Locate every blood parasite and identify its species.
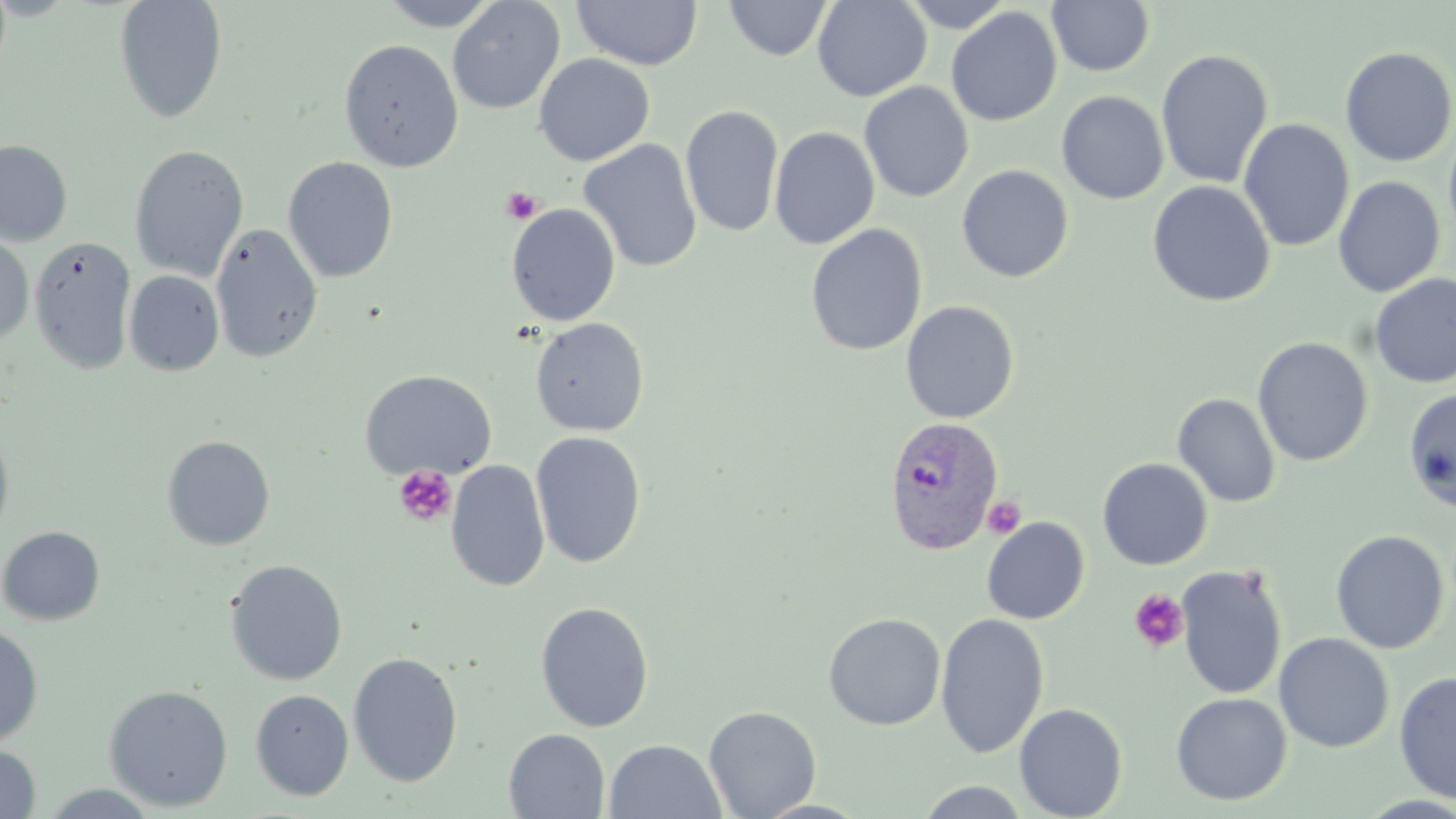
Approximate bounding boxes as (x1, y1, x2, y2) in pixels.
Plasmodium vivax-infected red blood cells: (883, 416, 1004, 554).
No Plasmodium falciparum, Plasmodium ovale, Plasmodium malariae, Babesia divergens, or Trypanosoma brucei observed.

Summary:
  - Platelet locations: (501, 186, 543, 225), (393, 465, 457, 527), (981, 495, 1026, 539), (1129, 589, 1189, 653)
  - Uninfected red blood cell locations: (379, 0, 500, 30), (447, 0, 565, 115), (724, 0, 833, 61), (812, 0, 932, 102), (899, 0, 1014, 33), (1047, 0, 1155, 77), (113, 1, 228, 123), (572, 1, 702, 70), (945, 6, 1063, 128), (338, 39, 464, 171), (1339, 45, 1456, 167), (1156, 48, 1273, 189), (533, 54, 655, 166), (858, 82, 974, 202), (1057, 91, 1169, 204), (680, 104, 784, 238), (1238, 119, 1354, 252), (1443, 120, 1456, 245), (769, 126, 880, 250), (0, 139, 73, 246), (578, 139, 703, 273), (129, 144, 249, 282), (283, 157, 399, 283), (956, 164, 1074, 283), (1333, 176, 1445, 298), (1148, 180, 1275, 307), (506, 204, 621, 326), (211, 223, 323, 364), (805, 224, 928, 356), (0, 231, 35, 345), (30, 235, 136, 374), (124, 270, 224, 376), (1369, 272, 1456, 390), (901, 300, 1020, 423), (529, 317, 649, 436), (1253, 337, 1374, 467), (359, 369, 497, 481), (1402, 387, 1456, 513), (1172, 393, 1280, 507), (0, 419, 16, 549), (530, 431, 647, 568), (161, 435, 276, 551), (1097, 457, 1213, 570), (445, 459, 550, 592), (981, 517, 1090, 624), (0, 526, 105, 626), (1330, 530, 1449, 654), (225, 559, 348, 685), (1175, 563, 1289, 700), (535, 601, 654, 732), (823, 612, 946, 730), (935, 612, 1050, 758), (0, 625, 43, 746), (1273, 632, 1394, 753), (348, 651, 464, 787), (1394, 670, 1456, 803), (103, 684, 233, 811), (250, 689, 354, 800), (1171, 692, 1292, 806), (1013, 703, 1128, 819), (703, 705, 822, 819), (504, 729, 610, 818), (604, 739, 726, 819), (0, 743, 41, 818), (914, 781, 1034, 817), (36, 783, 165, 818), (753, 798, 873, 819)
  - Slide-level diagnosis: Plasmodium vivax
  - Preparation: thin blood film
  - Stain: May-Grünwald-Giemsa
  - Magnification: 1000x
  - Image size: 1456×819 pixels
  - Field of view: single
  - Modality: light microscopy